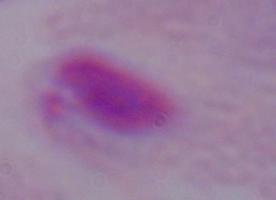
Summary:
  - Modality: micrograph
  - Magnification: 1000x
  - Identification: trichomonad